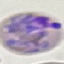

Summary:
  - Result: malaria parasites detected
  - Image type: automatically extracted cell patch, resized to 64 × 64 pixels
  - Preparation: thin smear
  - Capture: smartphone camera at the microscope eyepiece
  - Stain: Giemsa